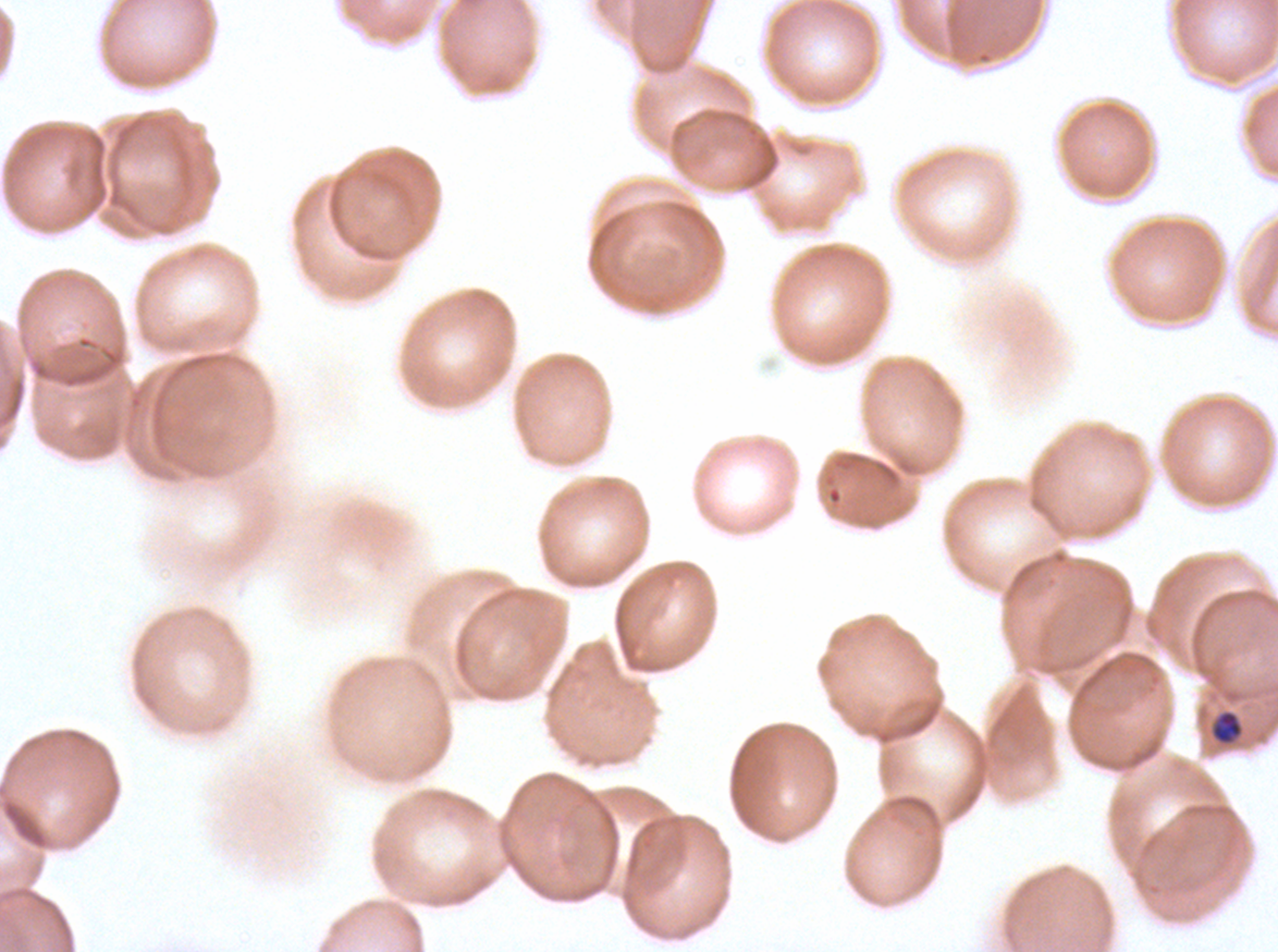
Approximate bounding boxes as {x1, y1, x2, y2} in pixels. Late-ring/early-trophozoite locations: {1211, 710, 1243, 744}. Thin blood film. Giemsa stain. One sub-image of a larger composite. Image is 1278×952 pixels. P. falciparum from a patient in The Gambia, cultured ex vivo for 24 to 48 hours.